Report the malaria status of this cell.
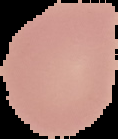

It is uninfected.

image size = 118×139 pixels
preparation = thin blood smear
image type = segmented cell region with the area outside set to black